Assess this cell for malaria.
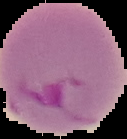
Parasitized.

Image is 127×139 pixels. Segmented cell region on a black background. From a thin blood film.